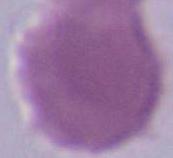

Summary:
  - Identification: erythrocyte
  - Magnification: 1000x
  - Modality: photomicrograph